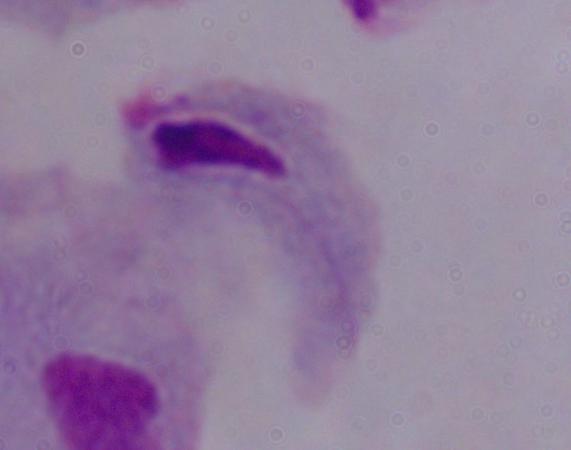

Summary:
  - Identification: trichomonad
  - Magnification: 1000x
  - Modality: micrograph